Assess the morphology of the red blood cells.
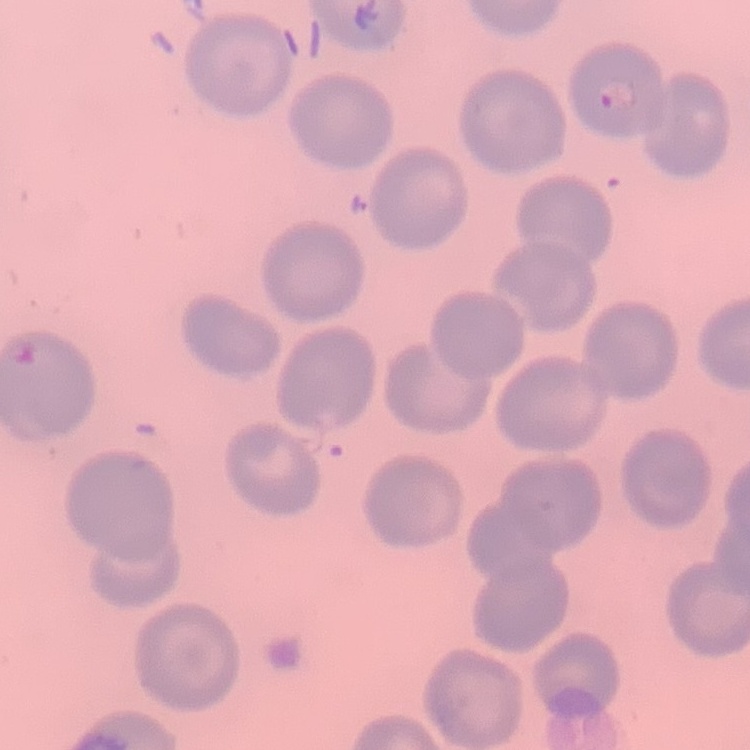
They show no rouleaux formation.

Square crop of a larger photomicrograph. Thin blood smear. Field's or Giemsa stain.